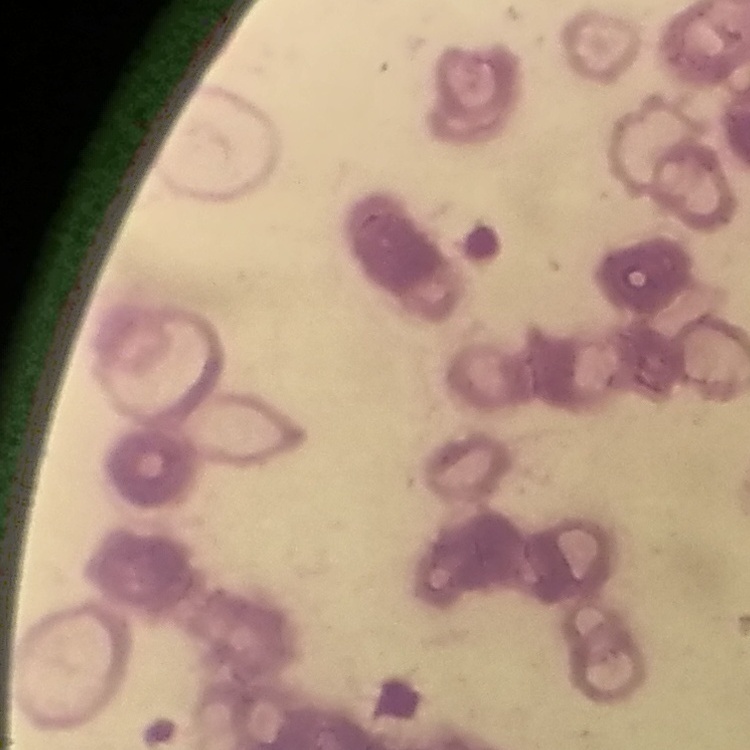

The red blood cells exhibit rouleaux formation. One tile cut from a larger photomicrograph. Field's or Giemsa stain. Thin blood smear.